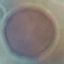
Result: negative for malaria parasites. Giemsa-stained preparation. Thin blood film. Acquired by smartphone through the microscope eyepiece. Cell patch, automatically extracted from a larger field of view and resized to 64 × 64 pixels.